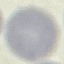
Result: no malaria parasites detected. Thin smear of blood. Giemsa stain. Automatically extracted cell patch, resized to 64 × 64 pixels. Acquired by smartphone through the microscope eyepiece.